Comment on the morphology of the erythrocytes.
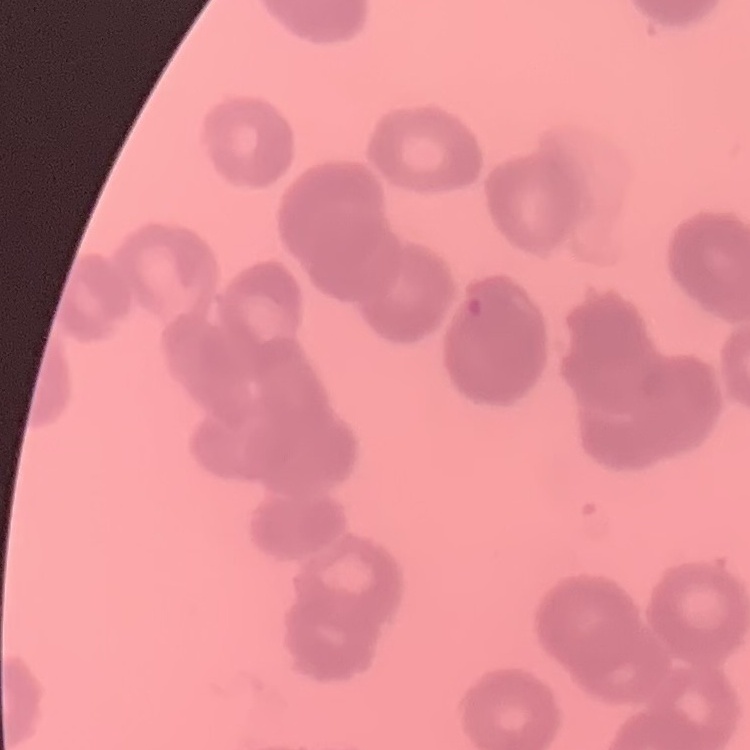
Rouleaux formation.

Square crop of a larger photomicrograph. Thin blood smear. Stained with either Field's or Giemsa.